Assess the morphology of the erythrocytes.
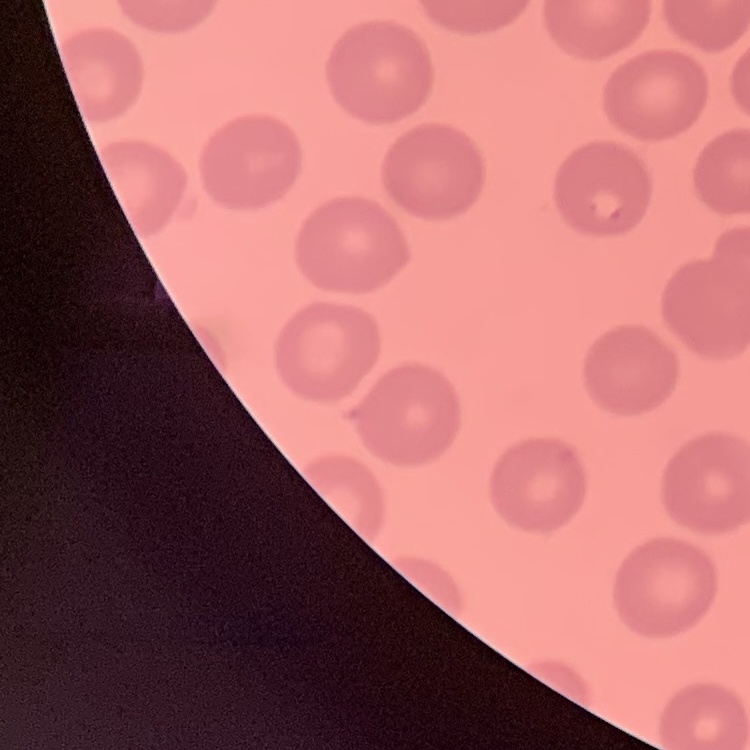
They show no rouleaux formation.

preparation = thin peripheral smear
stain = Field's or Giemsa
image type = one tile cut from a larger photomicrograph